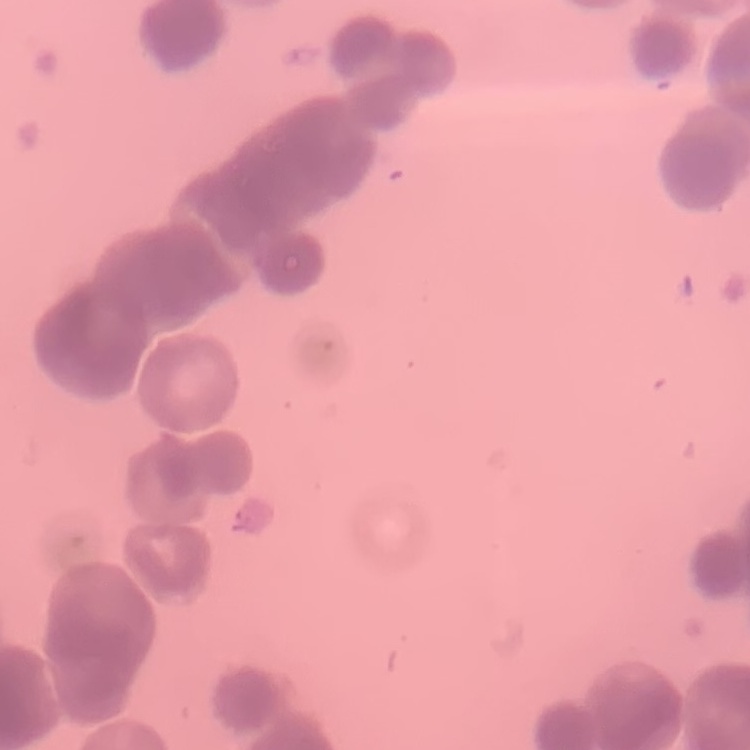
red_blood_cell_morphology: rouleaux formation
image_type: one tile cut from a larger photomicrograph
preparation: thin blood smear
stain: Field's or Giemsa